Assess the morphology of the red blood cells.
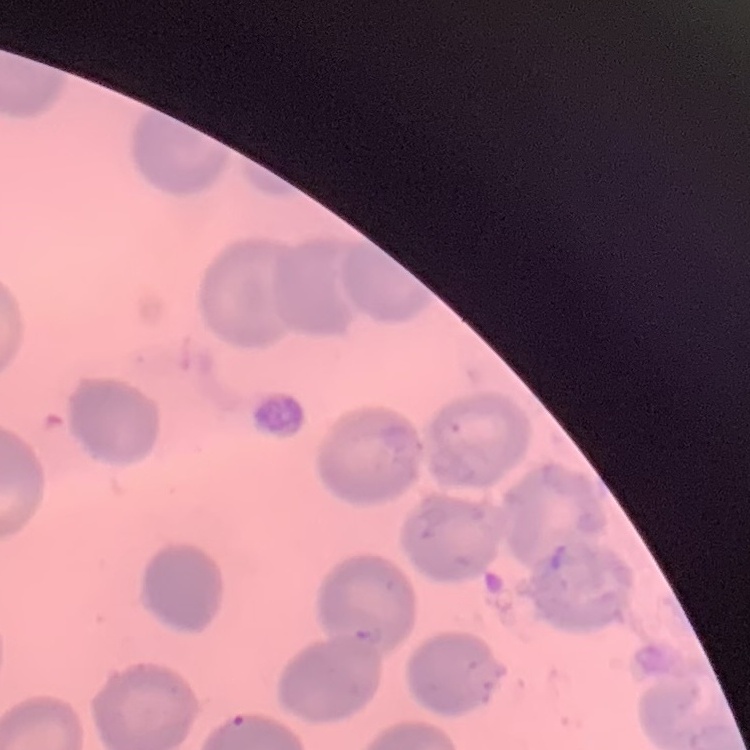
They show no rouleaux formation.

Stained with either Field's or Giemsa. Thin blood smear. One tile cut from a larger photomicrograph.